State which cell type is depicted.
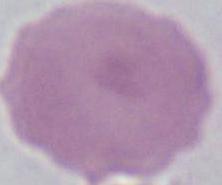

This is an erythrocyte.

Photomicrograph. 1000x magnification.